Point out each malaria parasite and each leukocyte.
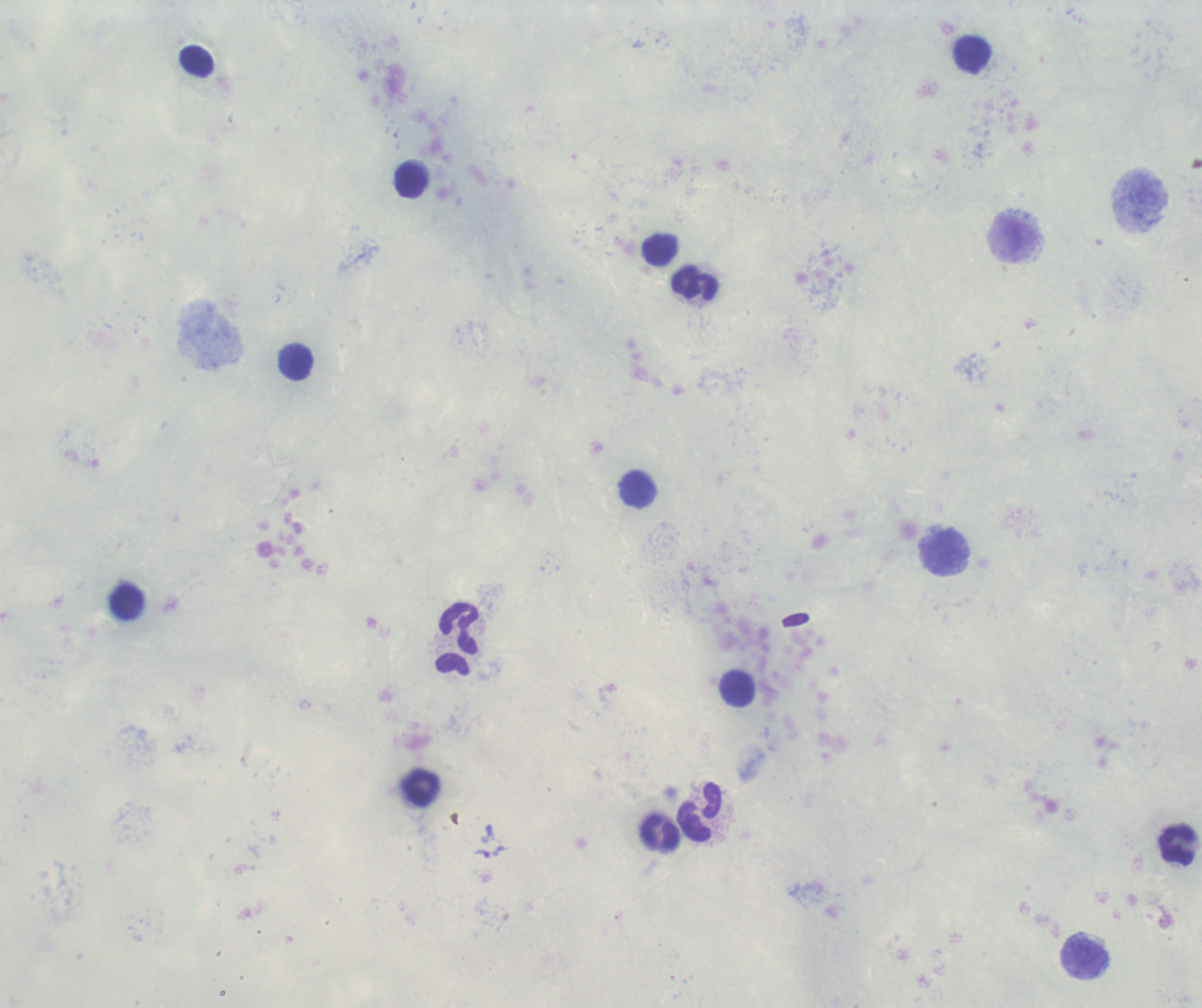

Approximate object centers, in pixels from the top-left corner.
Trophozoites: (x=483, y=854).
No schizont or gametocyte forms observed.
Leukocytes: (x=973, y=54), (x=196, y=61), (x=411, y=181), (x=1013, y=239), (x=661, y=250), (x=696, y=283), (x=295, y=362), (x=638, y=490), (x=945, y=551), (x=457, y=640), (x=738, y=689), (x=421, y=788), (x=699, y=812), (x=660, y=832), (x=1178, y=845), (x=1085, y=957).

{
  "field_of_view": "single",
  "coloration_quality": "good",
  "stain": "Romanowsky",
  "preparation": "thick blood smear",
  "image_size": "1202×1008 pixels",
  "magnification": "100x",
  "background_quality": "poor",
  "context": "previously used in a real diagnosis"
}